Name the parasite shown.
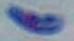
Toxoplasma gondii.

modality: photomicrograph
magnification: 1000x